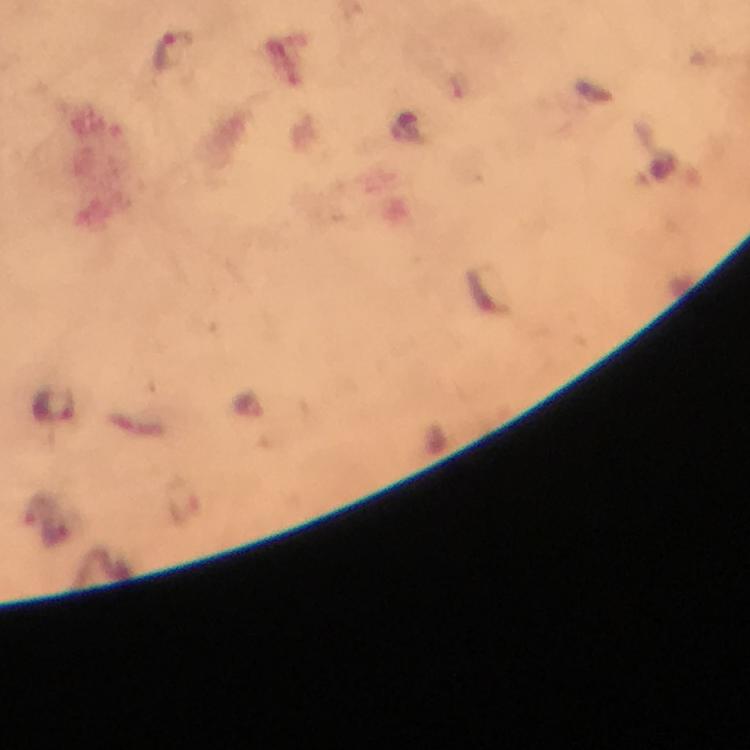

Approximate centers as (x, y) in pixels.
Summary:
  - Plasmodium parasite locations: (171, 51)
  - Cropped from: one field of view
  - Capture: smartphone camera through the microscope
  - Image size: 750×750 pixels
  - Magnification: 100x
  - Immersion oil: used
  - Preparation: thick blood smear
  - Context: from a diagnostic examination for malaria
  - Stain: Giemsa